Assess this cell for malaria.
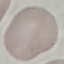

It is uninfected.

Summary:
  - Capture: smartphone through the microscope eyepiece
  - Image type: automatically extracted cell patch, resized to 64 × 64 pixels
  - Stain: Giemsa
  - Preparation: thin smear